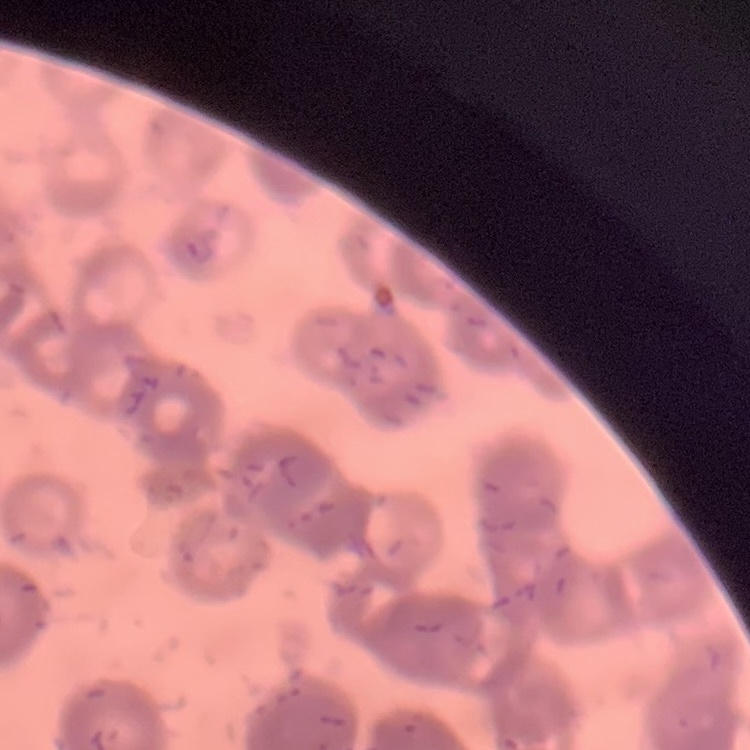
The red blood cells exhibit rouleaux formation. Thin blood film. Field's or Giemsa stain. Square crop of a larger photomicrograph.